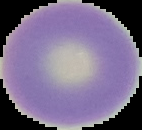
preparation = thin blood film
image type = segmented cell region on a black background
result = no malaria parasites seen
image size = 142×130 pixels